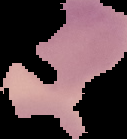

image type = segmented cell region with the area outside set to black
image size = 127×139 pixels
malaria status = uninfected
preparation = thin blood smear